Give the position of every malaria parasite.
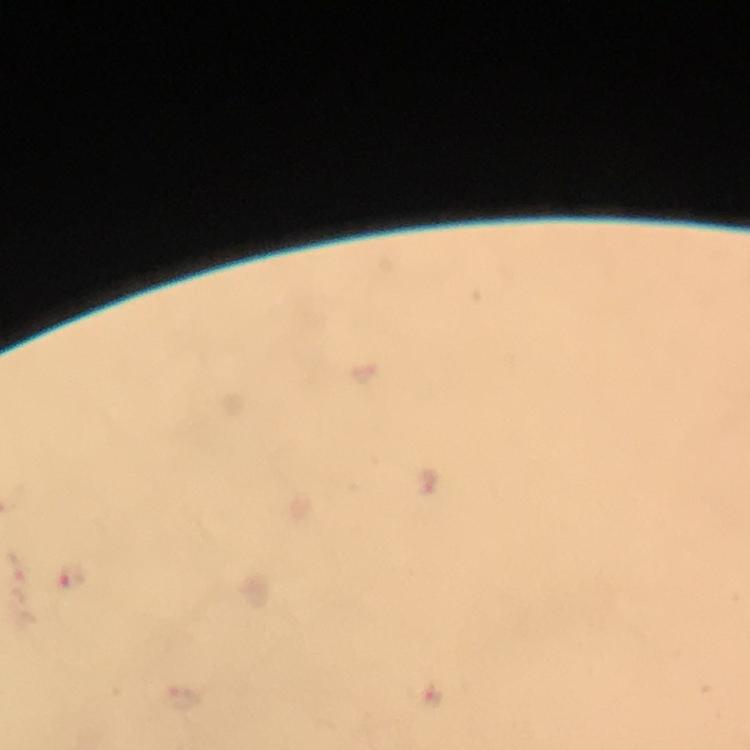
Approximate centers as (x, y) in pixels.
Malaria parasites: (70, 579).

Photographed with a smartphone mounted on the microscope. At 100x magnification. Giemsa stain. A crop from one field of view. Image is 750×750 pixels. Thick blood smear. Immersion oil applied. From a malaria diagnostic workup.